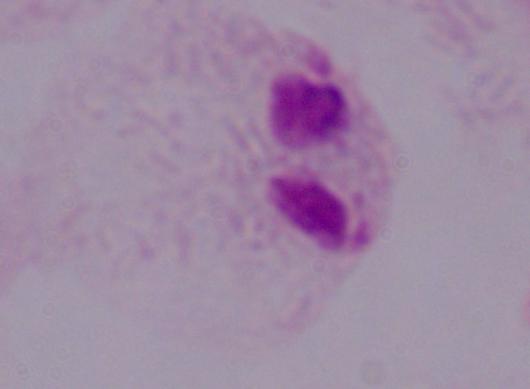
Summary:
  - Magnification: 1000x
  - Modality: micrograph
  - Identification: trichomonad